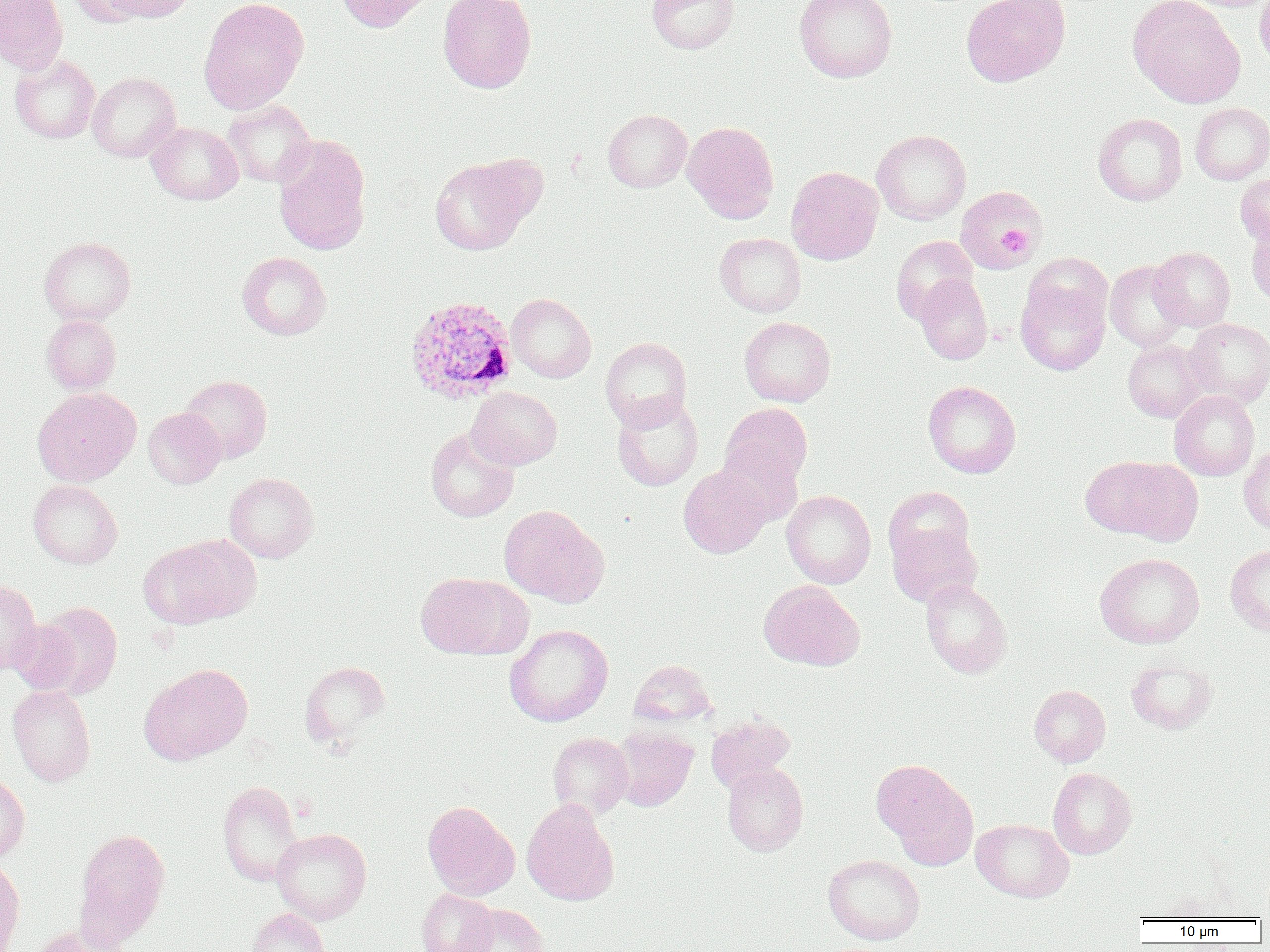

slide-level diagnosis = Plasmodium ovale
image size = 1270×952 pixels
field of view = single
magnification = 1000x
platelet locations = approximate bounding boxes as (x1,y1)-(x2,y2) corner pairs in pixels: (997,225)-(1033,258)
uninfected red blood cell locations = approximate bounding boxes as (x1,y1)-(x2,y2) corner pairs in pixels: (0,0)-(68,74), (68,0)-(152,26), (106,0)-(196,23), (199,0)-(309,113), (336,0)-(435,33), (438,0)-(536,93), (647,0)-(739,54), (794,0)-(897,82), (1254,0)-(1270,71), (961,1)-(1070,87), (1128,1)-(1246,108), (10,54)-(101,144), (87,72)-(180,162), (222,100)-(316,188), (1190,102)-(1270,185), (603,109)-(692,192), (1093,113)-(1187,205), (147,122)-(243,205), (682,122)-(779,223), (871,130)-(971,225), (273,135)-(371,255), (429,156)-(534,255), (786,166)-(883,265), (1235,172)-(1270,246), (955,186)-(1043,272), (1246,223)-(1270,308), (715,233)-(806,317), (891,236)-(978,324), (39,237)-(136,325), (1150,247)-(1235,331), (237,252)-(331,340), (1104,260)-(1189,352), (915,273)-(992,364), (1015,279)-(1110,375), (506,293)-(596,383), (41,314)-(121,394), (739,316)-(836,406), (1183,318)-(1270,407), (600,337)-(691,429), (1122,339)-(1208,423), (180,375)-(272,462), (923,380)-(1021,478), (467,386)-(562,470), (33,387)-(140,486), (1169,390)-(1260,481), (611,394)-(703,491), (720,402)-(813,490), (143,408)-(226,489), (425,428)-(519,522), (716,443)-(803,527), (1239,444)-(1270,535), (1080,456)-(1188,541), (678,466)-(771,558), (224,472)-(318,563), (27,480)-(122,569), (883,486)-(976,570), (781,490)-(876,588), (499,504)-(608,607), (888,525)-(981,607), (138,537)-(253,629), (1225,545)-(1270,636), (1095,553)-(1204,648), (415,571)-(531,660), (921,578)-(1012,678), (0,579)-(41,674), (759,580)-(865,671), (33,603)-(123,700), (8,618)-(83,696), (504,624)-(613,727), (1125,657)-(1218,734), (629,660)-(717,728), (299,661)-(390,748), (140,663)-(252,765), (7,685)-(96,787), (1029,685)-(1111,767), (706,714)-(795,793), (611,726)-(697,811), (548,733)-(634,818), (873,760)-(977,866), (722,763)-(808,855), (1047,767)-(1137,859), (0,774)-(30,861), (217,782)-(304,886), (521,799)-(619,906), (422,801)-(520,901), (971,818)-(1073,902), (75,828)-(171,945), (272,828)-(372,924), (823,854)-(925,945), (0,859)-(25,952), (417,889)-(498,952), (460,904)-(550,952), (246,908)-(329,952), (28,924)-(132,952)
Plasmodium ovale-infected red blood cell locations = approximate bounding boxes as (x1,y1)-(x2,y2) corner pairs in pixels: (404,295)-(518,405)
modality = light microscopy
preparation = thin blood smear